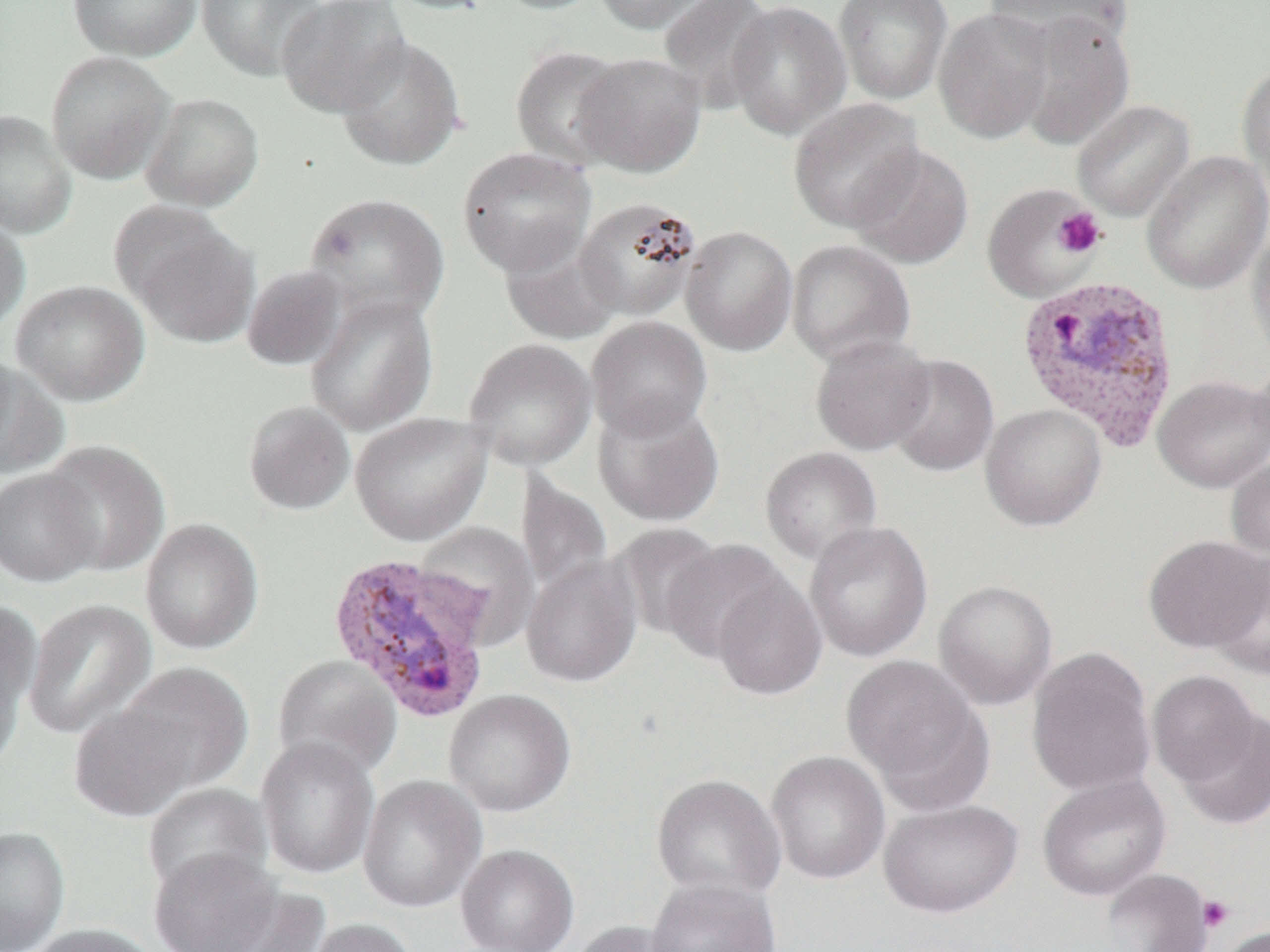

slide-level diagnosis = Plasmodium vivax
field of view = one of a larger specimen
uninfected red blood cell locations = approximate bounding boxes as (x1, y1, x2, y2) in pixels: (67, 0, 202, 61), (196, 0, 326, 81), (276, 0, 411, 117), (380, 0, 501, 15), (490, 0, 607, 15), (593, 0, 727, 35), (656, 0, 778, 111), (726, 0, 852, 140), (833, 0, 953, 104), (983, 0, 1136, 53), (933, 7, 1055, 143), (1011, 10, 1136, 150), (335, 36, 466, 171), (509, 45, 631, 170), (45, 50, 174, 184), (573, 51, 707, 177), (1236, 60, 1270, 198), (140, 92, 264, 212), (788, 98, 925, 233), (1072, 99, 1195, 221), (0, 109, 77, 238), (850, 145, 974, 269), (457, 146, 596, 278), (1142, 150, 1270, 294), (982, 183, 1103, 303), (303, 192, 450, 323), (575, 196, 703, 320), (0, 211, 30, 338), (127, 217, 259, 348), (1248, 223, 1270, 363), (680, 225, 798, 356), (499, 236, 623, 345), (786, 239, 916, 366), (241, 265, 349, 371), (10, 279, 150, 406), (304, 292, 439, 436), (586, 316, 713, 440), (810, 334, 936, 456), (463, 338, 598, 471), (886, 353, 999, 478), (1252, 357, 1270, 467), (0, 359, 69, 481), (1153, 375, 1270, 492), (593, 397, 725, 527), (242, 400, 356, 516), (980, 404, 1106, 531), (350, 412, 492, 546), (39, 439, 170, 577), (760, 446, 883, 566), (1225, 457, 1270, 561), (0, 468, 102, 587), (516, 474, 612, 599), (140, 518, 264, 655), (804, 520, 933, 662), (415, 522, 541, 648), (609, 523, 724, 640), (1143, 535, 1269, 653), (659, 539, 790, 665), (1206, 551, 1269, 677), (521, 555, 642, 688), (710, 572, 827, 700), (933, 580, 1058, 709), (0, 597, 42, 743), (23, 598, 156, 739), (1027, 646, 1157, 797), (842, 653, 992, 806), (271, 655, 402, 779), (117, 662, 253, 793), (1146, 670, 1261, 787), (444, 688, 575, 817), (68, 704, 197, 822), (1173, 709, 1270, 830), (255, 736, 380, 880), (765, 750, 890, 885), (651, 773, 786, 903), (1037, 773, 1171, 902), (358, 774, 487, 913), (141, 782, 272, 899), (877, 799, 1023, 918), (0, 826, 70, 951), (455, 843, 579, 952), (149, 848, 282, 952), (1098, 868, 1215, 952), (646, 876, 781, 952), (205, 886, 332, 952), (299, 918, 421, 952), (569, 920, 690, 952), (24, 922, 160, 952), (1215, 925, 1269, 952)
magnification = 1000x
preparation = thin blood smear
Plasmodium vivax-infected red blood cell locations = approximate bounding boxes as (x1, y1, x2, y2) in pixels: (1014, 275, 1182, 451), (326, 551, 496, 724)
platelet locations = approximate bounding boxes as (x1, y1, x2, y2) in pixels: (1053, 207, 1106, 258), (1198, 895, 1234, 932)
image size = 1270×952 pixels
modality = light microscopy